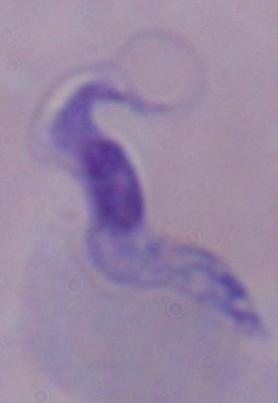 A trypanosome is shown. Captured at 1000x magnification. Photomicrograph.